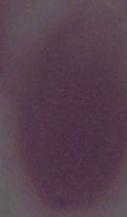

identification = red blood cell
modality = photomicrograph
magnification = 1000x